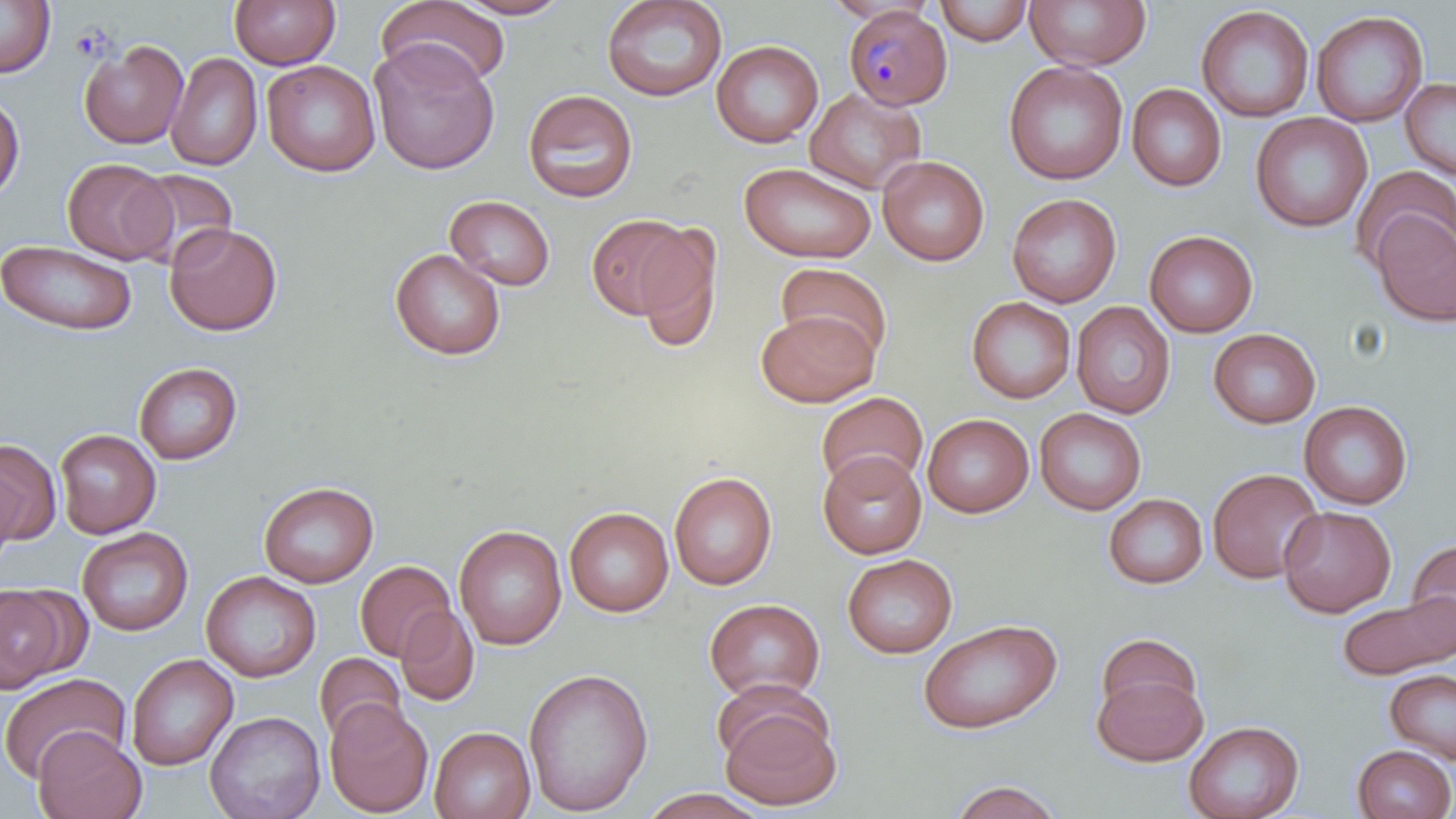

slide-level diagnosis = Plasmodium malariae
platelet locations = approximate bounding boxes as (x1,y1)-(x2,y2) corner pairs in pixels: (70,24)-(112,62)
uninfected red blood cell locations = approximate bounding boxes as (x1,y1)-(x2,y2) corner pairs in pixels: (0,0)-(55,77), (229,0)-(340,70), (452,0)-(572,19), (601,0)-(728,103), (822,0)-(937,24), (1024,0)-(1151,71), (377,1)-(512,88), (934,1)-(1035,46), (1195,5)-(1314,122), (1310,10)-(1428,127), (369,39)-(501,175), (79,40)-(188,149), (711,40)-(824,148), (165,52)-(263,171), (261,60)-(381,177), (1003,60)-(1128,185), (1400,77)-(1456,180), (1126,84)-(1227,191), (805,87)-(926,195), (522,89)-(638,203), (0,94)-(24,201), (1250,112)-(1372,232), (877,155)-(990,266), (62,158)-(175,264), (739,162)-(877,264), (1350,165)-(1456,274), (127,169)-(238,269), (1007,193)-(1122,308), (445,195)-(555,291), (1372,211)-(1456,327), (586,212)-(697,320), (165,222)-(282,336), (635,223)-(722,353), (1144,229)-(1259,337), (0,241)-(138,336), (390,249)-(506,360), (775,262)-(894,364), (966,296)-(1076,404), (1071,301)-(1176,418), (756,309)-(879,407), (1208,327)-(1321,429), (133,361)-(242,465), (815,391)-(929,494), (1299,400)-(1413,510), (1034,407)-(1146,515), (922,414)-(1034,517), (54,428)-(161,538), (0,438)-(61,546), (817,451)-(927,559), (0,464)-(22,570), (1207,468)-(1324,584), (668,471)-(777,590), (259,481)-(378,587), (1104,493)-(1208,589), (1278,506)-(1396,617), (564,507)-(674,617), (454,524)-(567,650), (77,527)-(193,636), (1406,537)-(1456,650), (842,554)-(958,658), (354,560)-(456,662), (200,571)-(321,682), (0,584)-(71,691), (1337,592)-(1456,680), (704,598)-(825,703), (395,606)-(480,706), (917,619)-(1062,735), (1094,632)-(1204,727), (314,652)-(406,745), (126,653)-(238,771), (522,666)-(654,816), (1092,669)-(1208,767), (1385,669)-(1456,765), (0,672)-(131,783), (718,698)-(842,811), (323,699)-(434,817), (204,710)-(326,819), (1183,720)-(1304,819), (429,726)-(535,819), (33,728)-(146,818), (1352,744)-(1455,819), (947,780)-(1065,818), (638,788)-(770,818)
field of view = single
stain = May-Grünwald-Giemsa
modality = optical microscopy
Plasmodium malariae-infected red blood cell locations = approximate bounding boxes as (x1,y1)-(x2,y2) corner pairs in pixels: (844,6)-(953,110)
image size = 1456×819 pixels
preparation = thin blood smear
magnification = 1000x